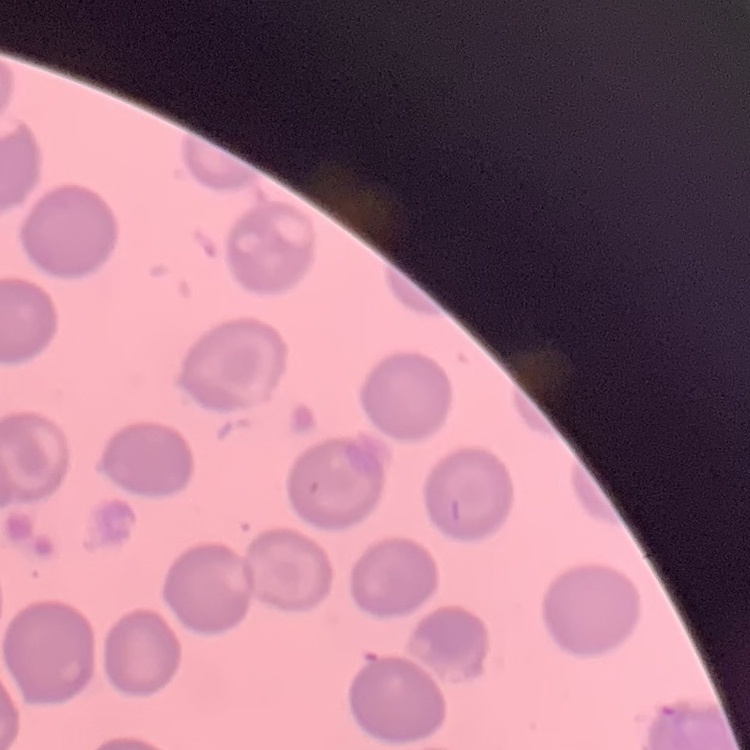

The red blood cells show no rouleaux formation. Field's or Giemsa stain. Thin blood smear. One tile cut from a larger photomicrograph.